Classify this cell by malaria status.
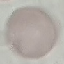

It is uninfected.

Cell patch, automatically extracted from a larger field of view and resized to 64 × 64 pixels. Acquired by smartphone through the microscope eyepiece. Thin blood film. Giemsa-stained preparation.